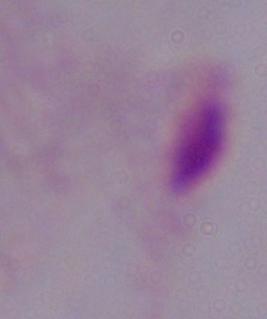

modality: micrograph
magnification: 1000x
identification: trichomonad